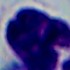 A leukocyte is shown. 1000x magnification. Micrograph.